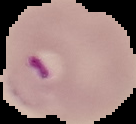

image size = 136×124 pixels
image type = segmented cell region with the area outside set to black
preparation = thin blood film
malaria status = parasitized